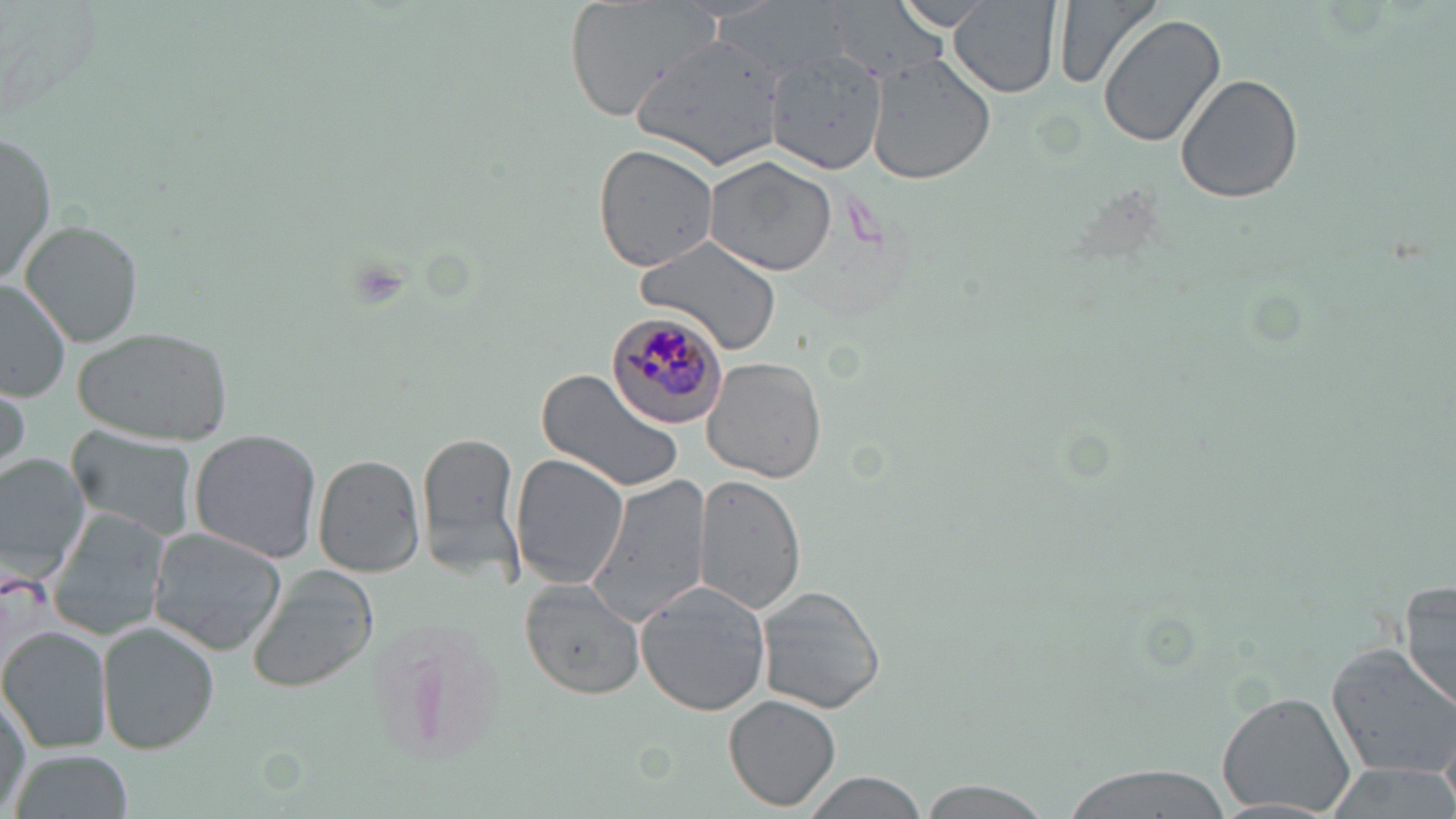
Summary:
  - Coordinate format: approximate bounding boxes as [x1, y1, x2, y2] in pixels
  - Uninfected red blood cell locations: [564, 0, 722, 119], [952, 0, 1062, 97], [1054, 0, 1162, 90], [889, 2, 1000, 32], [1097, 13, 1226, 149], [632, 32, 788, 173], [766, 49, 888, 172], [868, 55, 996, 183], [1175, 70, 1305, 206], [0, 129, 56, 289], [592, 142, 720, 272], [704, 154, 840, 277], [21, 221, 143, 348], [635, 235, 782, 354], [0, 281, 73, 404], [73, 325, 236, 446], [702, 356, 827, 483], [534, 366, 687, 495], [0, 375, 29, 478], [65, 428, 201, 543], [188, 429, 323, 564], [418, 429, 526, 584], [0, 452, 92, 582], [509, 453, 629, 590], [312, 455, 425, 578], [695, 474, 808, 614], [587, 475, 712, 626], [47, 507, 172, 644], [146, 527, 286, 654], [245, 565, 379, 694], [520, 580, 647, 700], [1400, 581, 1456, 712], [635, 585, 774, 716], [757, 586, 886, 714], [99, 625, 218, 753], [0, 628, 112, 754], [1324, 642, 1456, 777], [1, 689, 32, 811], [1215, 689, 1357, 814], [724, 694, 842, 811], [6, 748, 135, 819], [1056, 762, 1232, 819], [1318, 762, 1456, 819], [800, 773, 934, 819], [914, 778, 1058, 818]
  - Plasmodium malariae-infected red blood cell locations: [607, 308, 734, 428]
  - Slide-level diagnosis: Plasmodium malariae
  - Field of view: one of a larger specimen
  - Magnification: 1000x
  - Image size: 1456×819 pixels
  - Preparation: thin blood smear
  - Modality: light microscopy
  - Stain: May-Grünwald-Giemsa